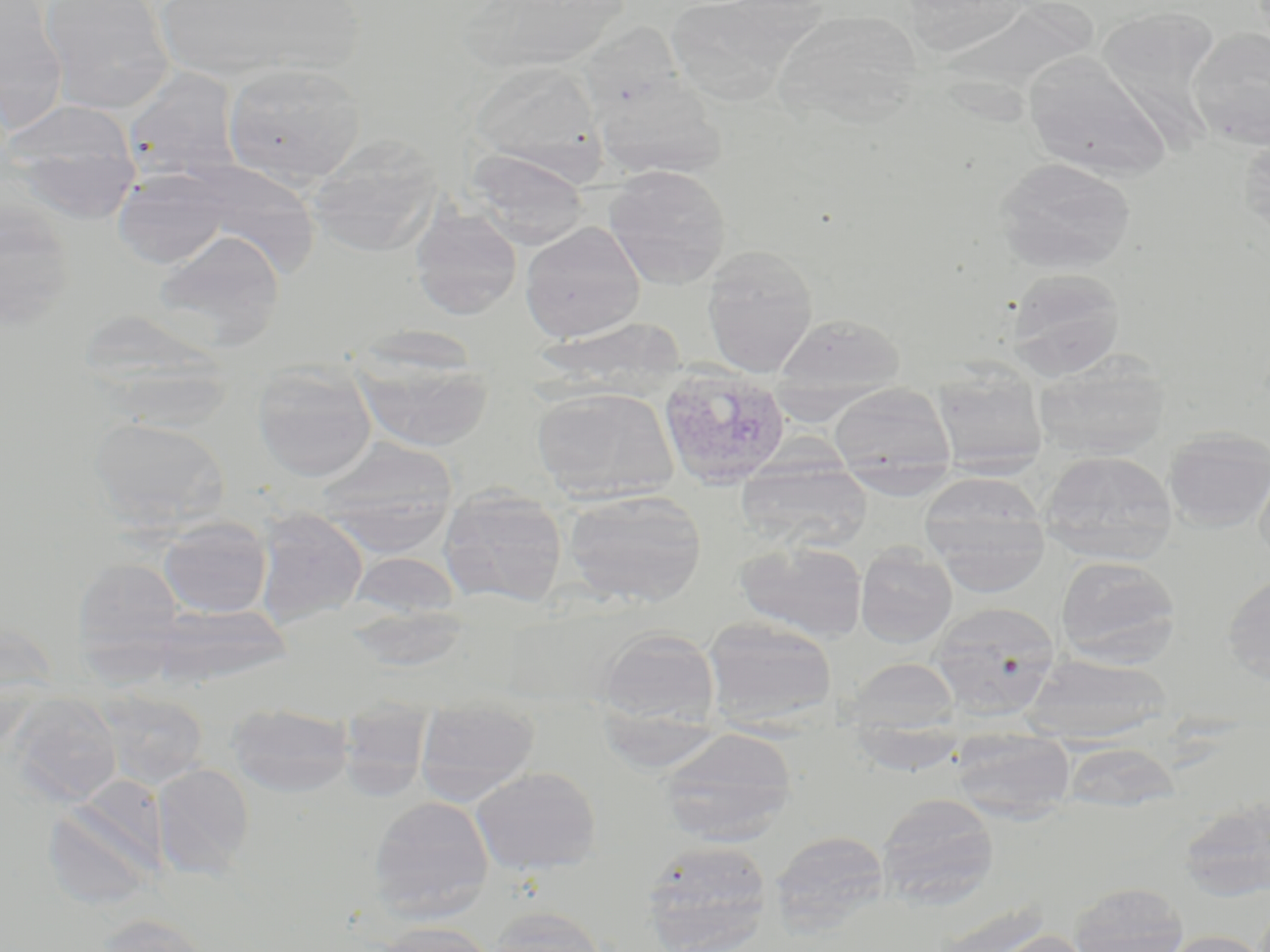

slide-level diagnosis = Plasmodium vivax
magnification = 1000x
Plasmodium vivax-infected red blood cell locations = approximate bounding boxes as (x1, y1, x2, y2) in pixels: (658, 366, 791, 489)
field of view = one of a larger specimen
modality = optical microscopy
image size = 1270×952 pixels
preparation = thin blood film
stain = May-Grünwald-Giemsa
uninfected red blood cell locations = approximate bounding boxes as (x1, y1, x2, y2) in pixels: (39, 0, 174, 114), (147, 0, 361, 82), (461, 0, 632, 72), (0, 1, 69, 133), (673, 2, 832, 112), (941, 3, 1099, 126), (1097, 5, 1222, 141), (770, 9, 923, 128), (579, 25, 686, 121), (1188, 28, 1270, 150), (1024, 55, 1170, 181), (467, 60, 602, 170), (223, 61, 366, 187), (122, 66, 243, 182), (595, 77, 726, 180), (3, 99, 141, 219), (306, 134, 442, 256), (1237, 136, 1270, 244), (466, 150, 591, 247), (994, 156, 1138, 275), (166, 160, 322, 277), (604, 165, 732, 289), (111, 166, 233, 270), (0, 201, 77, 332), (410, 205, 522, 319), (520, 221, 645, 343), (151, 228, 287, 348), (700, 246, 819, 377), (1005, 268, 1126, 379), (79, 311, 235, 424), (776, 313, 905, 396), (543, 316, 689, 396), (351, 333, 495, 454), (1033, 354, 1171, 460), (931, 360, 1049, 476), (252, 362, 377, 482), (829, 383, 955, 483), (532, 386, 678, 503), (89, 416, 229, 530), (1163, 427, 1270, 531), (317, 438, 459, 553), (1038, 450, 1177, 564), (1254, 456, 1270, 571), (736, 459, 872, 553), (919, 472, 1048, 564), (438, 485, 567, 608), (563, 489, 707, 607), (253, 508, 367, 627), (925, 509, 1051, 597), (158, 517, 272, 618), (736, 540, 868, 642), (855, 545, 957, 648), (348, 551, 462, 621), (1055, 555, 1181, 666), (72, 556, 185, 664), (1222, 573, 1270, 686), (929, 602, 1060, 719), (149, 603, 293, 687), (344, 604, 470, 672), (702, 617, 837, 729), (597, 628, 720, 731), (1024, 654, 1173, 742), (847, 658, 961, 740), (96, 689, 209, 789), (9, 696, 122, 805), (414, 699, 541, 803), (226, 703, 354, 797), (340, 714, 431, 797), (660, 728, 797, 846), (950, 730, 1074, 822), (1063, 741, 1178, 814), (153, 763, 254, 877), (471, 766, 600, 875), (877, 792, 999, 910), (368, 796, 494, 920), (1179, 798, 1270, 901), (42, 801, 158, 911), (770, 830, 889, 935), (642, 839, 773, 950), (1068, 881, 1189, 952), (485, 906, 611, 952), (91, 914, 208, 952), (375, 921, 496, 952), (983, 930, 1094, 952), (1158, 930, 1268, 952)